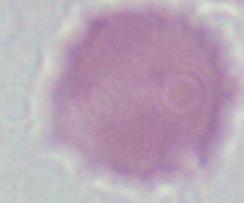
Photomicrograph. 1000x magnification. An erythrocyte is seen.